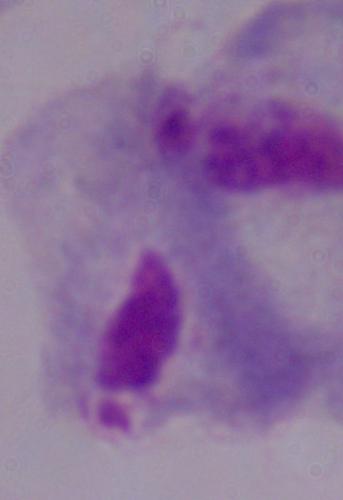
A trichomonad is shown. 1000x magnification. Photomicrograph.